Point out each leukocyte.
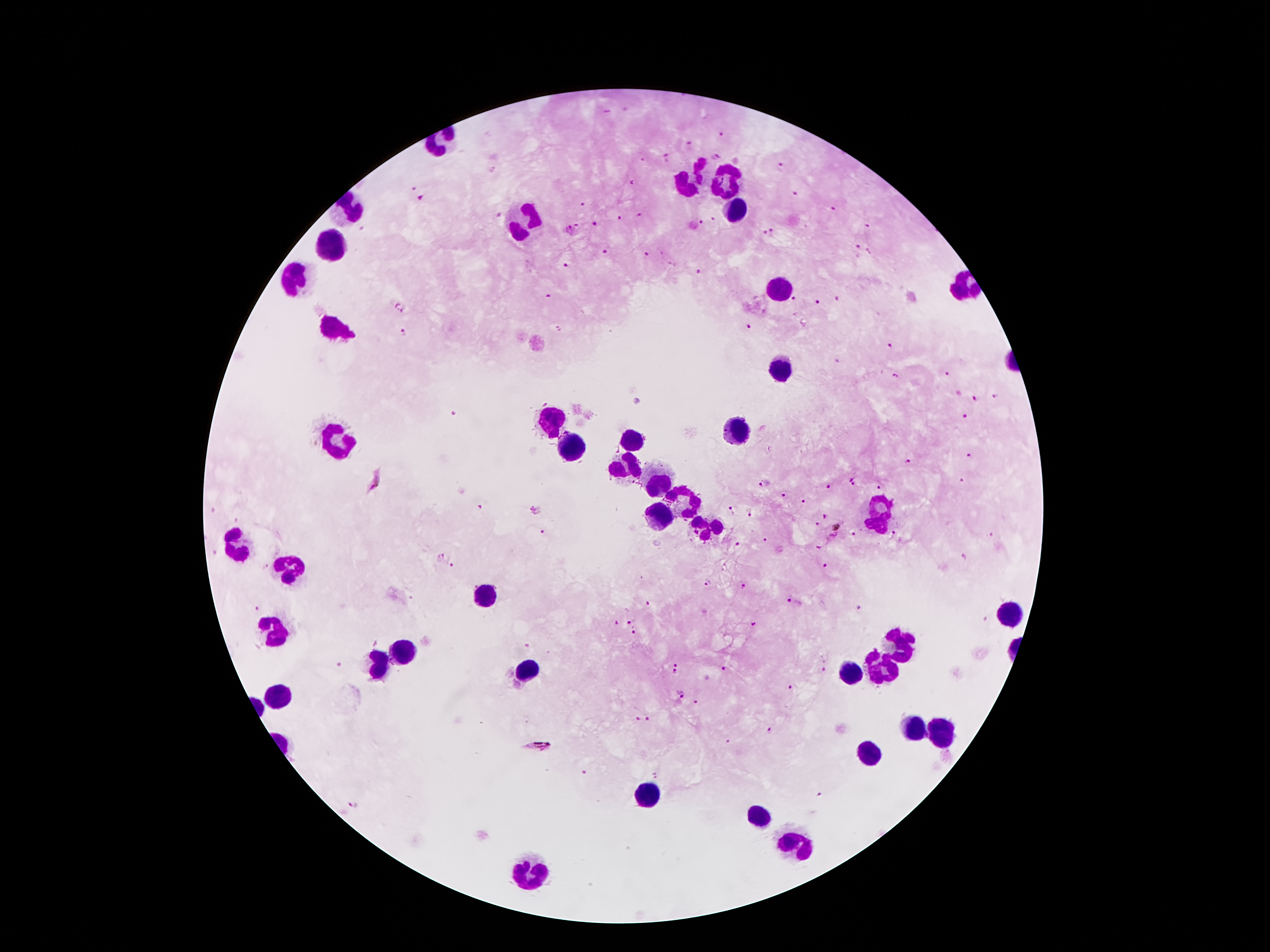

Approximate centers as [x, y] in pixels.
Leukocytes: [689, 180], [726, 180], [738, 208], [354, 212], [530, 222], [336, 247], [297, 276], [782, 285], [334, 324], [784, 369], [551, 420], [738, 429], [341, 439], [630, 443], [572, 450], [628, 469], [658, 483], [689, 500], [880, 514], [660, 516], [710, 526], [240, 546], [292, 567], [488, 596], [1011, 614], [273, 630], [899, 642], [401, 652], [378, 666], [875, 668], [528, 673], [849, 673], [283, 693], [912, 728], [941, 731], [868, 756], [646, 792], [759, 817], [794, 845], [530, 871].

Plasmodium parasite locations = [721, 135], [688, 143], [716, 155], [667, 157], [781, 168], [635, 182], [414, 185], [795, 193], [424, 199], [583, 203], [832, 209], [498, 216], [640, 216], [619, 219], [714, 220], [701, 223], [579, 225], [596, 226], [868, 226], [569, 230], [773, 230], [765, 233], [857, 246], [605, 251], [868, 251], [647, 255], [567, 265], [700, 270], [549, 297], [792, 299], [837, 299], [397, 300], [814, 301], [404, 312], [749, 326], [405, 331], [888, 346], [949, 374], [894, 375], [998, 396], [976, 400], [963, 417], [970, 455], [908, 460], [850, 476], [376, 479], [964, 480], [763, 481], [854, 485], [827, 486], [877, 486], [783, 495], [803, 501], [733, 508], [481, 509], [537, 511], [750, 514], [824, 517], [816, 522], [541, 532], [895, 532], [833, 533], [852, 533], [990, 533], [764, 539], [737, 544], [819, 548], [964, 555], [439, 556], [453, 566], [826, 566], [642, 579], [707, 584], [745, 587], [791, 600], [648, 603], [256, 608], [859, 608], [755, 622], [628, 623], [616, 624], [634, 635], [676, 661], [337, 664], [725, 666], [674, 673], [824, 673], [792, 685], [680, 694], [694, 702], [647, 718], [637, 719], [770, 729], [726, 742], [538, 744], [586, 773], [654, 775], [817, 795]
field of view = one from this slide
magnification = 100x
patient malaria status = infected with Plasmodium falciparum
stain = Giemsa
image size = 1270×952 pixels
preparation = thick blood film
capture = smartphone camera through the microscope eyepiece